Describe the morphology of the erythrocytes.
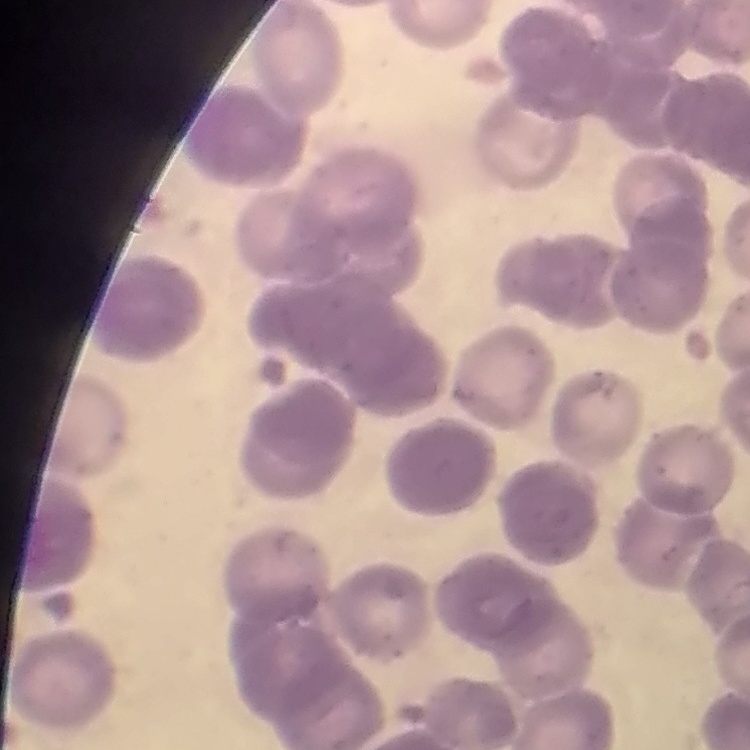

They show rouleaux formation.

One tile cut from a larger photomicrograph. Thin peripheral smear. Field's or Giemsa stain.